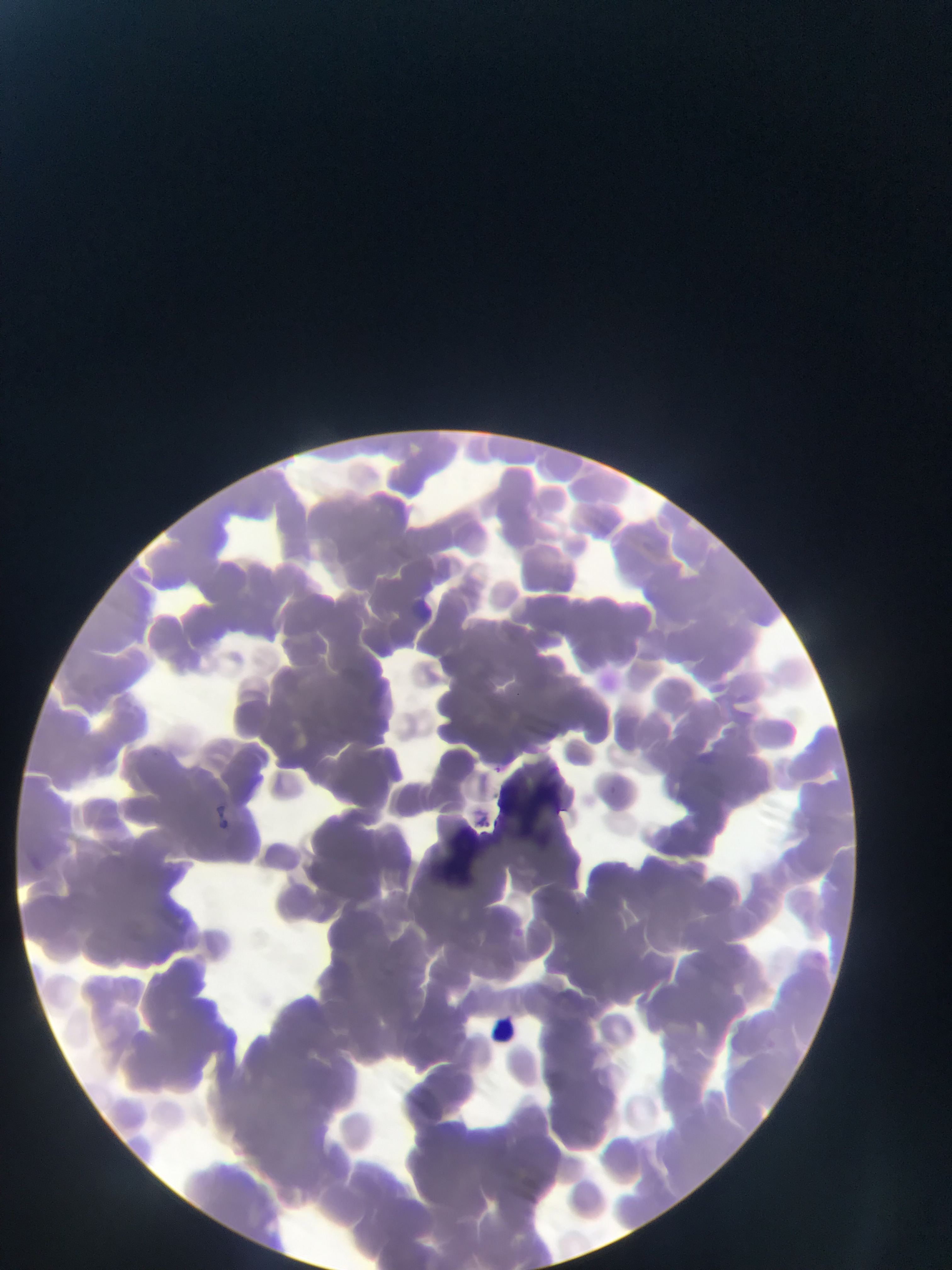 Approximate bounding boxes as {left, top, right, bottom} in pixels. Artifact (stain precipitate or debris) locations: {489, 751, 573, 827}, {446, 810, 482, 884}. Leukocyte locations: {488, 1009, 543, 1065}. Photographed through a microscope with a mobile-phone camera. Single field of view. Image is 952×1270 pixels. Collected in Ghana. Thin blood film.